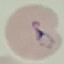

Result: malaria parasites identified. Photographed with a smartphone camera at the microscope eyepiece. Automatically extracted cell patch, resized to 64 × 64 pixels. Thin blood smear. Giemsa stain.